Assess this cell for malaria.
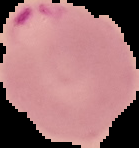

Parasitized.

Cell region segmented out of the field of view; the surrounding area is masked to black. From a thin blood smear. Image is 139×148 pixels.